Locate malaria parasites and leukocytes.
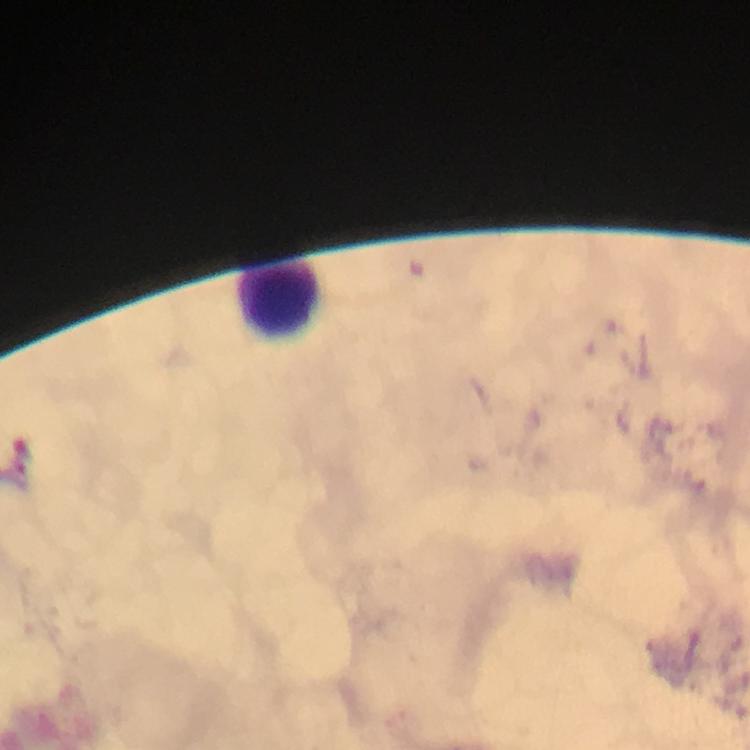
No malaria parasites seen.
Approximate centers as [x, y] in pixels.
Leukocytes: [280, 299].

magnification: 100x
immersion_oil: applied
cropped_from: a single field of view
context: from a diagnostic examination for malaria
capture: smartphone photograph through a microscope
stain: Giemsa
preparation: thick smear
image_size: 750×750 pixels